Name the cell type shown.
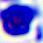

A leukocyte.

Summary:
  - Modality: photomicrograph
  - Magnification: 400x